Describe the morphology of the red blood cells.
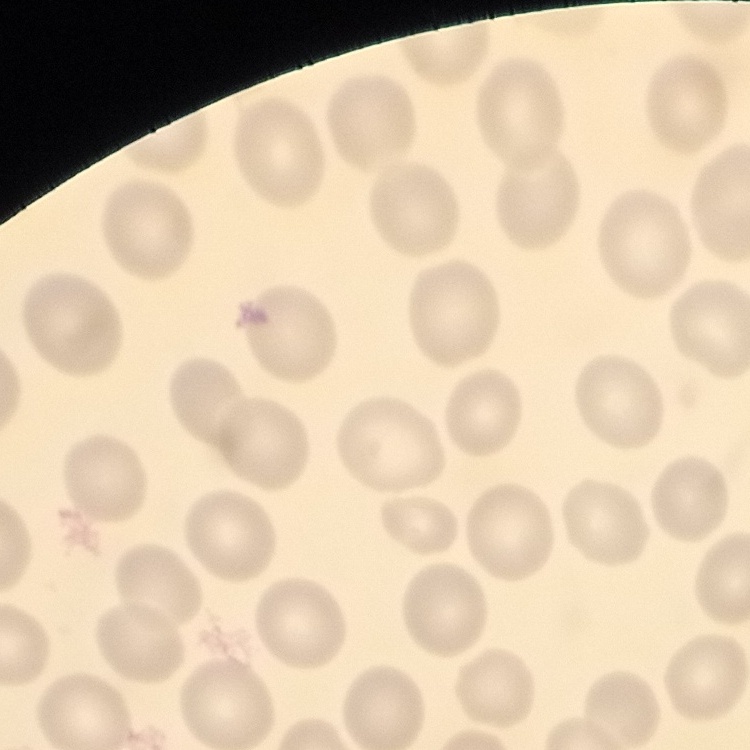
No rouleaux formation.

Summary:
  - Image type: square crop of a larger photomicrograph
  - Stain: Field's or Giemsa
  - Preparation: thin blood film